Report the malaria status of this cell.
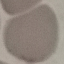
It is uninfected.

Summary:
  - Stain: Giemsa
  - Preparation: thin blood film
  - Capture: smartphone camera at the microscope eyepiece
  - Image type: automatically extracted cell patch, resized to 64 × 64 pixels